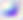 Photomicrograph. Toxoplasma gondii is shown. Captured at 400x magnification.